Report the malaria status.
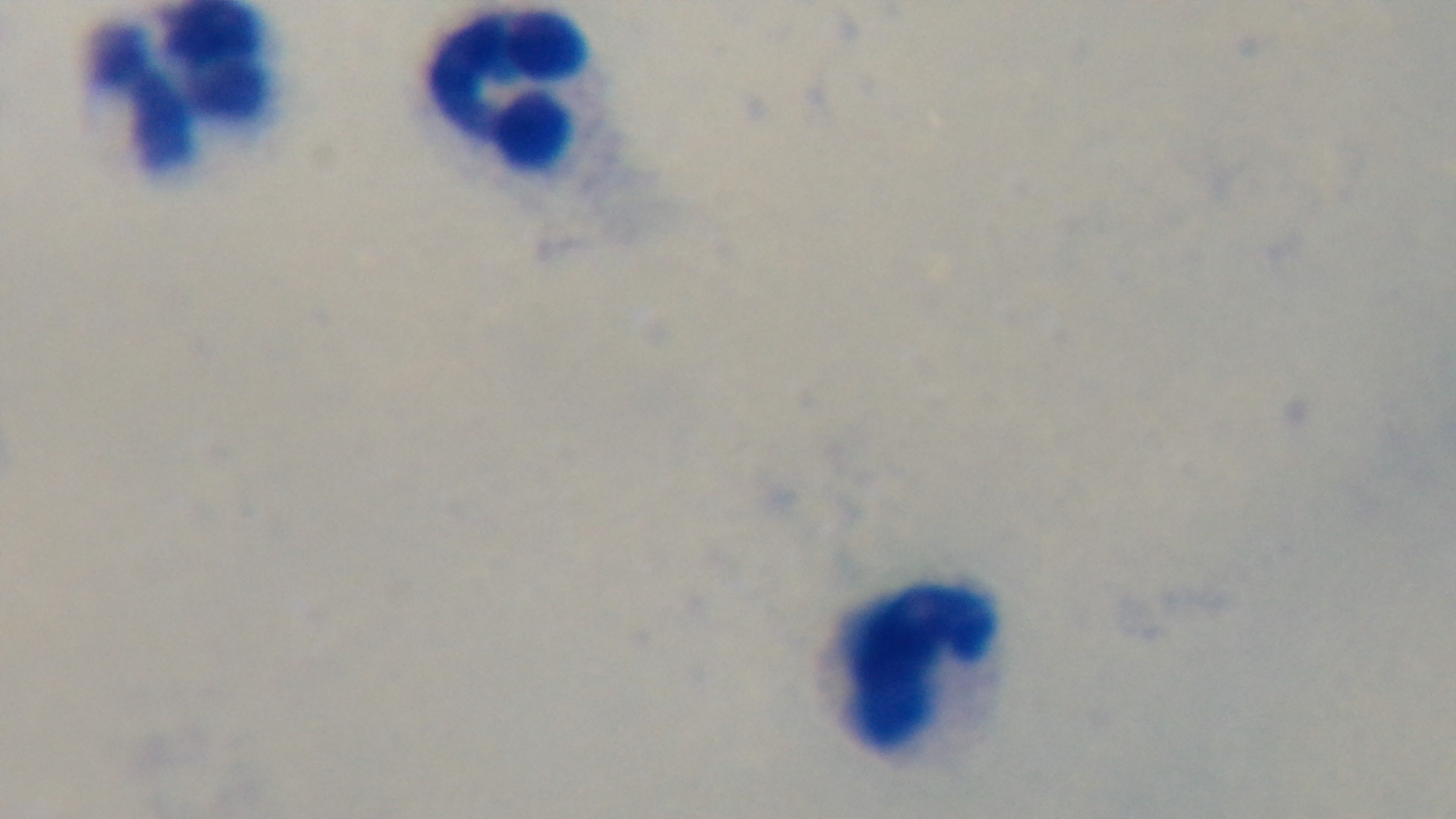
It is uninfected.

Single field of view. Giemsa stain. Captured with a mounted 4K digital camera. Preparation: thick smear. Light microscopy. Oil-immersion objective, 100x.